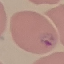

malaria status = parasitized
image type = cell patch, automatically extracted from a larger field of view and resized to 64 × 64 pixels
capture = smartphone through the microscope eyepiece
preparation = thin smear
stain = Giemsa